Assess this cell for malaria.
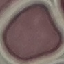
Uninfected.

Summary:
  - Stain: Giemsa
  - Preparation: thin blood film
  - Image type: automatically extracted cell patch, resized to 64 × 64 pixels
  - Capture: smartphone through the microscope eyepiece